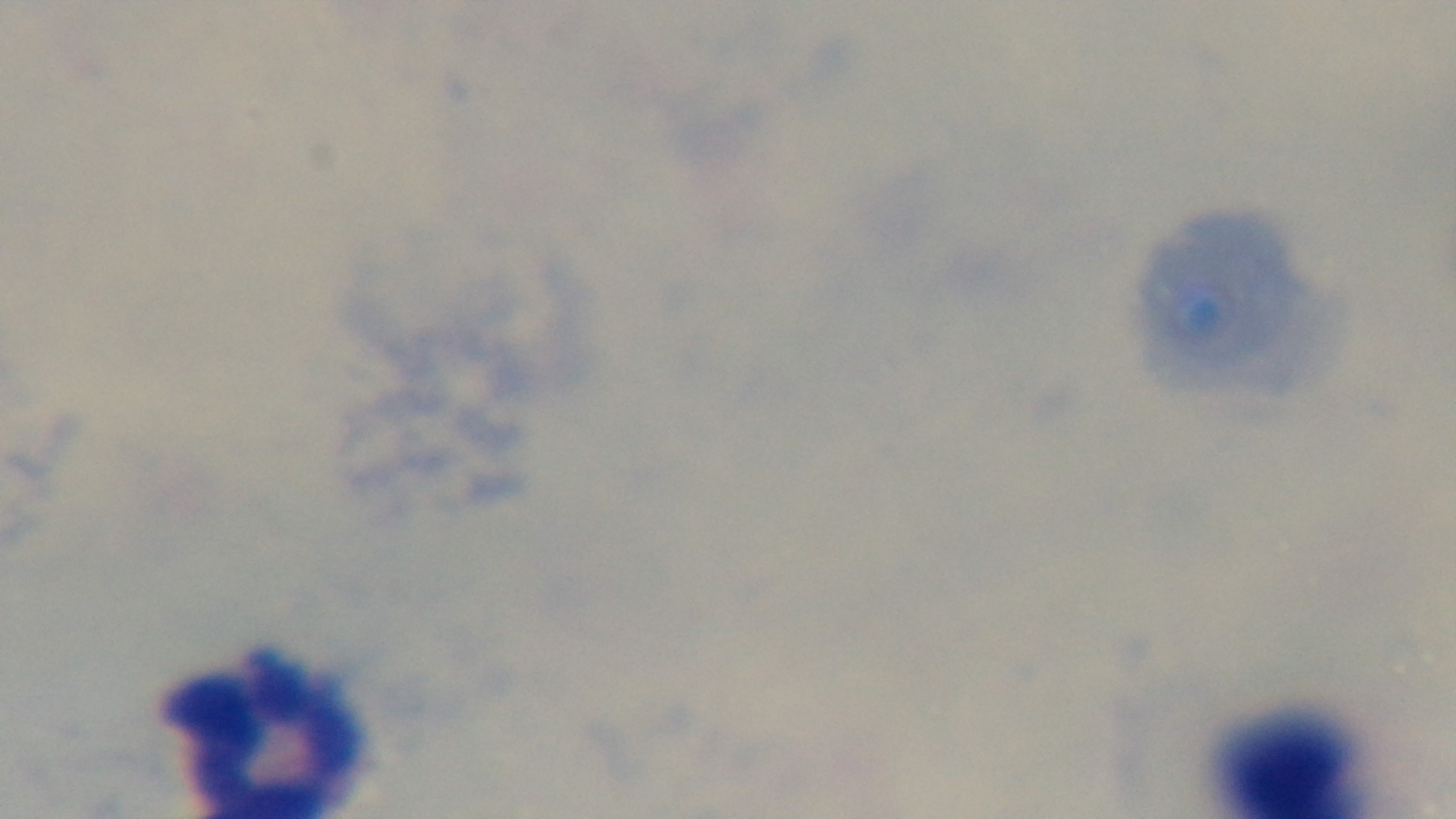 Oil-immersion objective, 100x. Captured with a mounted 4K digital camera. Malaria status: uninfected. Single field of view. Giemsa-stained. Preparation: thick blood film. Light microscopy.